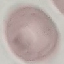
Malaria status: uninfected. Thin blood film. Photographed with a smartphone camera at the microscope eyepiece. Cell patch, automatically extracted from a larger field of view and resized to 64 × 64 pixels. Giemsa-stained preparation.